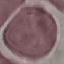
malaria status = uninfected
stain = Giemsa
preparation = thin blood film
capture = smartphone camera at the microscope eyepiece
image type = cell patch, automatically extracted from a larger field of view and resized to 64 × 64 pixels